Report the malaria status of this cell.
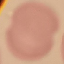
It is uninfected.

image type = cell patch, automatically extracted from a larger field of view and resized to 64 × 64 pixels
preparation = thin blood smear
capture = smartphone through the microscope eyepiece
stain = Giemsa